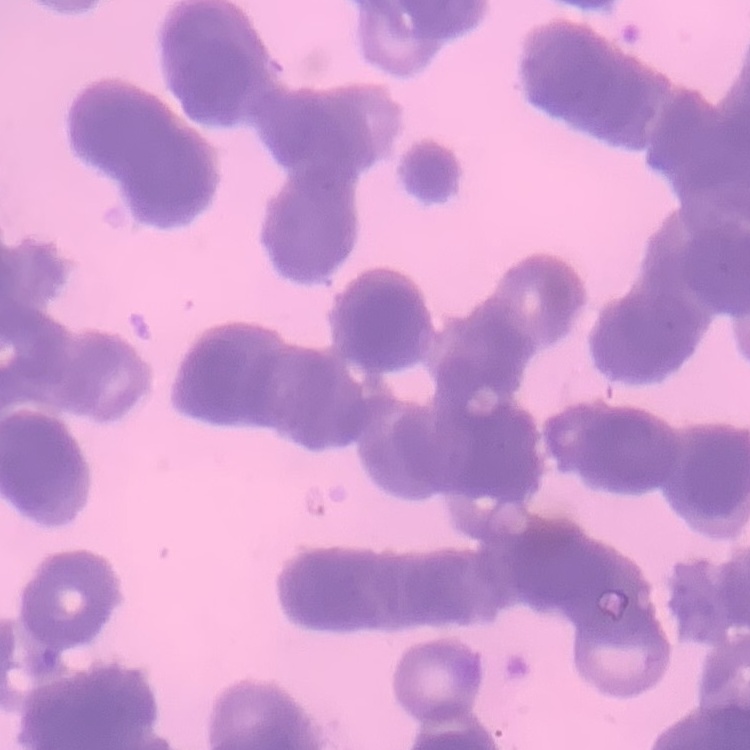

Summary:
  - Red blood cell morphology: rouleaux formation
  - Stain: Field's or Giemsa
  - Preparation: thin blood smear
  - Image type: one tile cut from a larger photomicrograph